Give the preparation type.
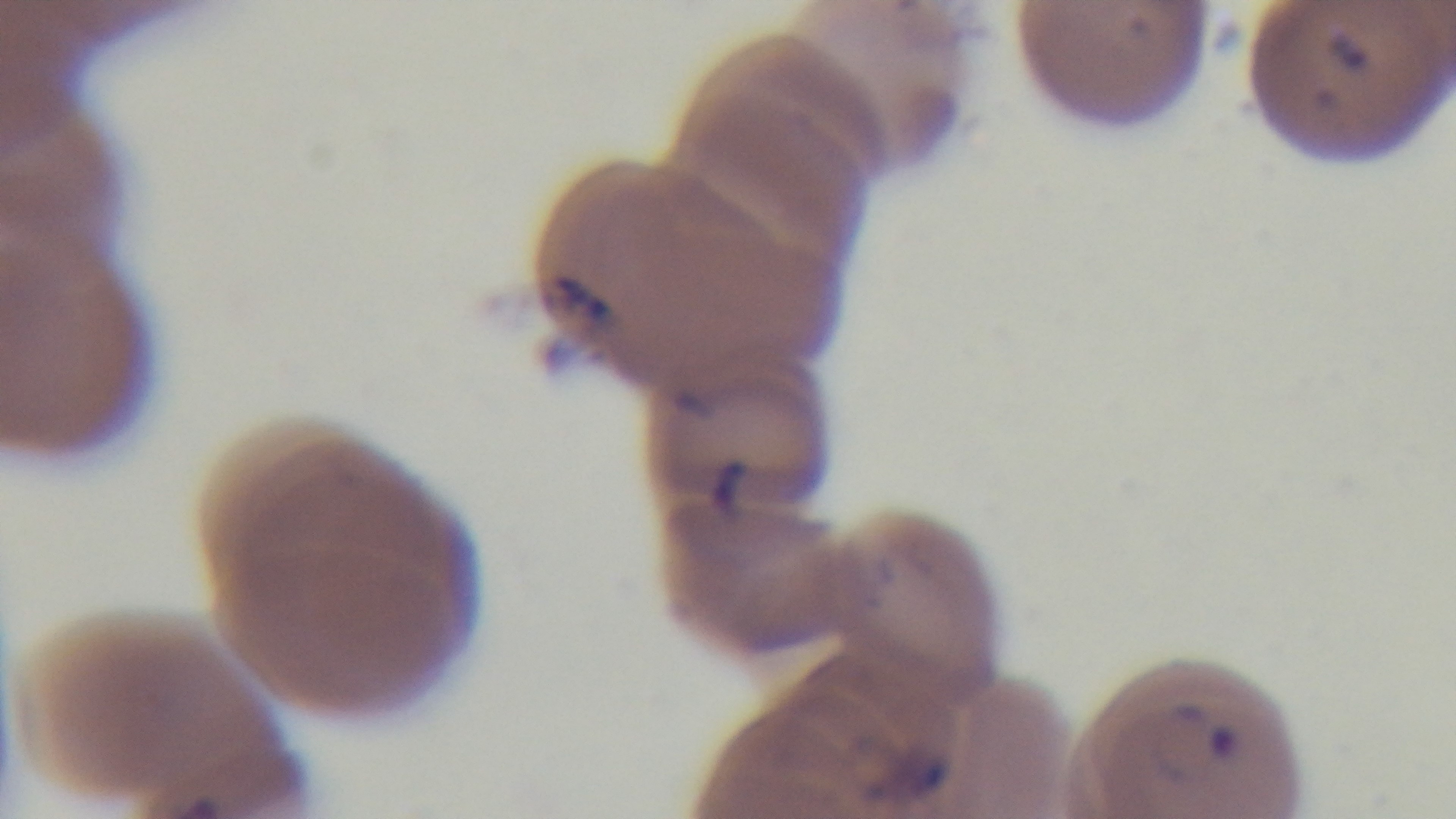

It is a thin blood film.

Single field of view. Photomicrograph. Giemsa stain. Malaria status: infected. Mounted 4K digital camera. Oil-immersion objective, 100x.